Identify the parasite.
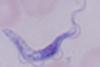
A trypanosome.

1000x magnification. Photomicrograph.